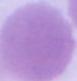

Summary:
  - Identification: erythrocyte
  - Modality: photomicrograph
  - Magnification: 1000x